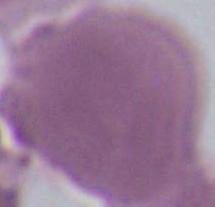
Micrograph. An erythrocyte is seen. 1000x magnification.